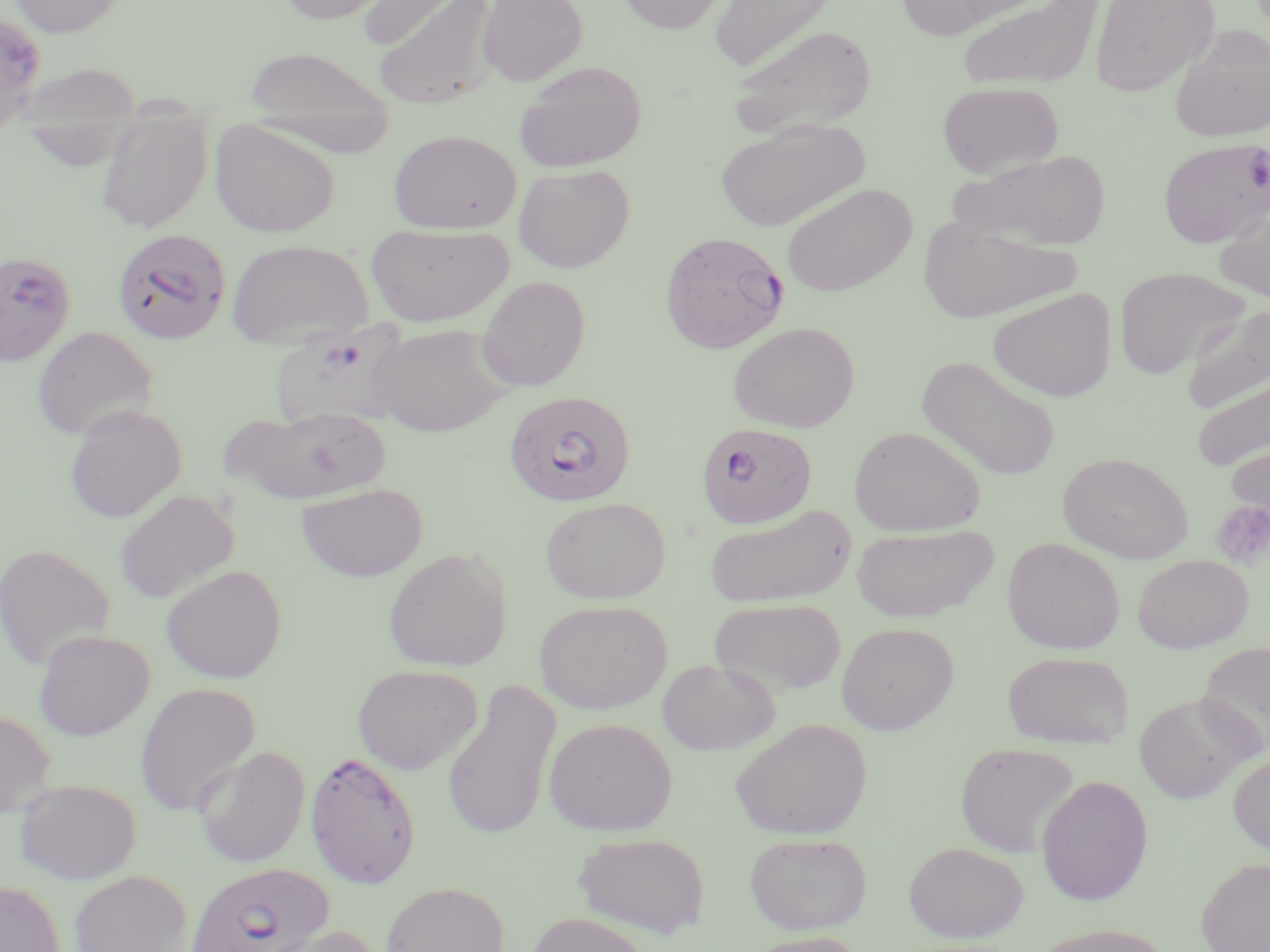
slide-level diagnosis = Plasmodium falciparum
image size = 1270×952 pixels
stain = May-Grünwald-Giemsa
magnification = 1000x
platelet locations = approximate bounding boxes as [x1, y1, x2, y2] in pixels: [1210, 501, 1270, 569]
preparation = thin blood smear
modality = light microscopy
uninfected red blood cell locations = approximate bounding boxes as [x1, y1, x2, y2] in pixels: [8, 0, 127, 38], [275, 0, 393, 24], [478, 0, 588, 86], [617, 0, 729, 34], [709, 0, 838, 74], [895, 0, 1028, 39], [957, 0, 1104, 92], [1088, 0, 1220, 97], [358, 1, 477, 51], [371, 1, 500, 110], [727, 24, 878, 137], [1168, 25, 1270, 143], [244, 46, 396, 150], [514, 61, 647, 171], [937, 81, 1064, 179], [94, 104, 213, 234], [209, 119, 341, 238], [715, 120, 867, 231], [388, 130, 522, 234], [949, 149, 1112, 252], [513, 164, 635, 272], [781, 182, 918, 297], [1212, 197, 1270, 304], [916, 216, 1080, 323], [365, 222, 514, 327], [226, 238, 374, 348], [1114, 266, 1251, 378], [476, 275, 591, 391], [987, 288, 1117, 402], [1182, 303, 1270, 414], [728, 321, 860, 433], [368, 322, 513, 436], [31, 325, 158, 441], [917, 354, 1062, 481], [1191, 372, 1270, 473], [63, 404, 186, 523], [218, 406, 389, 506], [849, 425, 985, 536], [1225, 439, 1270, 534], [1058, 452, 1193, 564], [295, 482, 428, 582], [114, 489, 239, 604], [539, 496, 671, 604], [705, 505, 856, 609], [851, 523, 998, 622], [1002, 537, 1125, 654], [0, 543, 116, 670], [383, 547, 512, 672], [1133, 554, 1253, 653], [161, 564, 287, 683], [709, 597, 846, 698], [534, 599, 671, 714], [836, 622, 959, 734], [34, 629, 154, 740], [1198, 640, 1270, 754], [1002, 651, 1134, 749], [656, 658, 780, 755], [351, 663, 483, 775], [442, 679, 561, 841], [134, 682, 261, 818], [1134, 693, 1254, 803], [0, 710, 57, 818], [543, 717, 677, 836], [730, 718, 871, 839], [954, 741, 1080, 857], [194, 745, 310, 868], [1228, 752, 1270, 856], [1036, 774, 1154, 905], [15, 778, 141, 884], [744, 831, 873, 935], [572, 832, 710, 938], [904, 841, 1028, 941], [1196, 857, 1270, 952], [68, 869, 195, 952], [0, 880, 65, 952], [380, 881, 510, 952], [525, 911, 654, 952], [255, 924, 385, 952], [1030, 924, 1174, 952], [737, 931, 869, 952]
Plasmodium falciparum-infected red blood cell locations = approximate bounding boxes as [x1, y1, x2, y2] in pixels: [0, 12, 46, 132], [1158, 137, 1270, 247], [111, 228, 232, 345], [658, 230, 790, 354], [0, 251, 76, 367], [269, 324, 412, 433], [503, 390, 636, 507], [696, 421, 817, 530], [304, 750, 421, 890], [184, 861, 333, 952]
field of view = one of a larger specimen